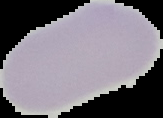

Summary:
  - Malaria status: uninfected
  - Image size: 163×118 pixels
  - Image type: cell region segmented out of the field of view; surrounding area masked to black
  - Preparation: thin blood smear